Report the malaria status of this cell.
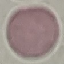

Uninfected.

Summary:
  - Capture: smartphone through the microscope eyepiece
  - Stain: Giemsa
  - Image type: cell patch, automatically extracted from a larger field of view and resized to 64 × 64 pixels
  - Preparation: thin blood film